Locate every blood parasite and identify its species.
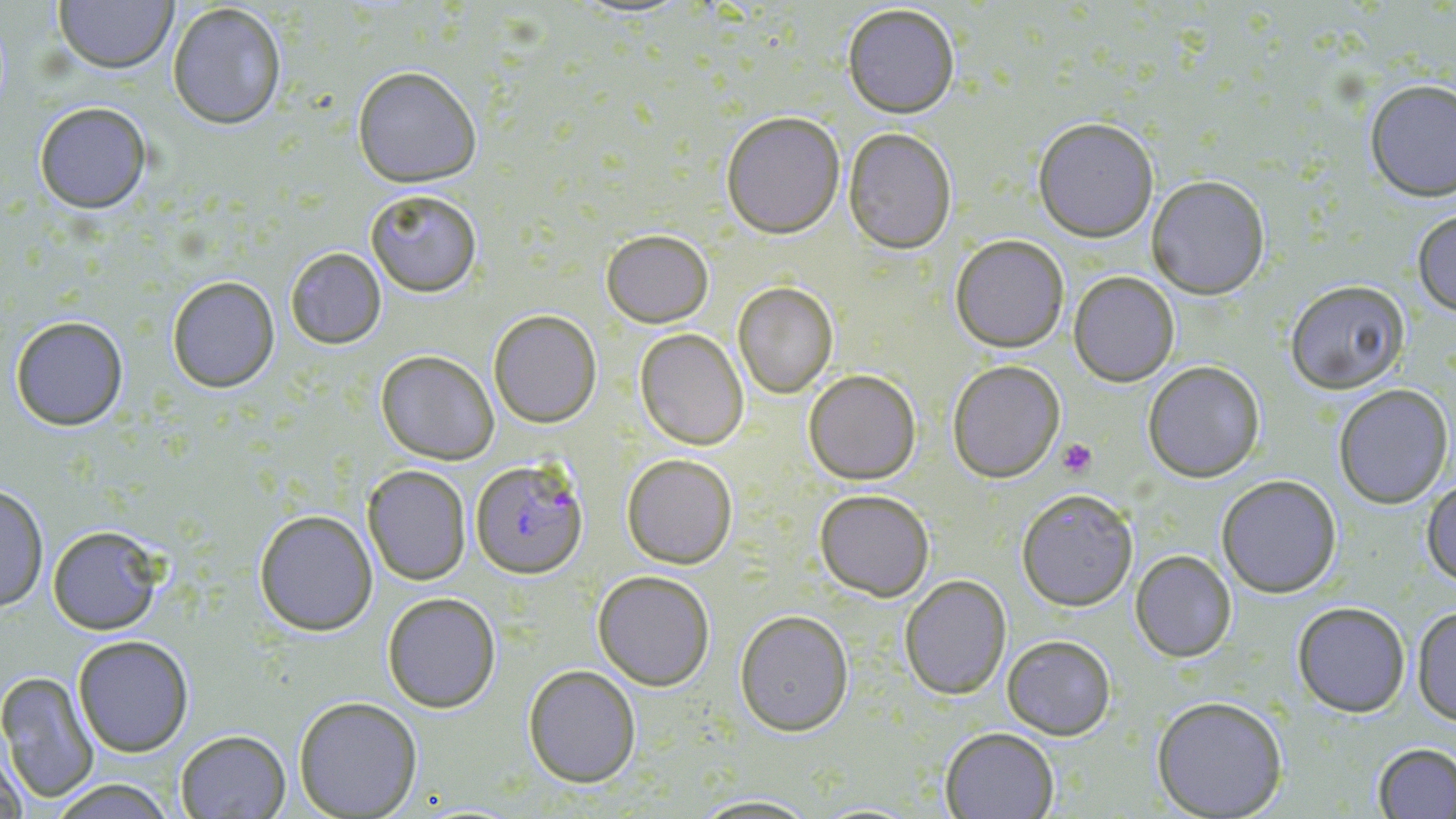
Approximate bounding boxes as (x1, y1, x2, y2) in pixels.
Plasmodium falciparum-infected red blood cells: (471, 458, 588, 578).
No Plasmodium ovale, Plasmodium malariae, Plasmodium vivax, Babesia divergens, or Trypanosoma brucei observed.

slide_level_diagnosis: Plasmodium falciparum
magnification: 1000x
preparation: thin blood film
uninfected_red_blood_cell_locations: 'approximate bounding boxes as (x1, y1, x2, y2) in pixels: (54, 0, 178, 74), (167, 3, 288, 130), (842, 3, 961, 117), (352, 65, 482, 187), (1364, 78, 1456, 201), (33, 101, 152, 213), (720, 111, 845, 238), (1033, 116, 1159, 242), (843, 127, 957, 254), (1147, 175, 1270, 299), (365, 188, 482, 296), (1412, 208, 1456, 317), (602, 229, 713, 328), (950, 234, 1069, 352), (285, 247, 386, 349), (1069, 271, 1179, 386), (166, 275, 280, 392), (1285, 279, 1409, 393), (732, 282, 838, 398), (489, 309, 602, 427), (10, 315, 129, 431), (634, 329, 749, 450), (376, 350, 499, 465), (947, 359, 1065, 482), (1142, 360, 1265, 482), (803, 369, 921, 485), (1333, 383, 1454, 509), (622, 453, 738, 568), (363, 464, 471, 586), (1216, 474, 1342, 598), (1422, 476, 1456, 586), (0, 483, 49, 612), (1017, 488, 1138, 611), (814, 489, 934, 601), (254, 509, 378, 636), (47, 525, 163, 634), (1130, 550, 1236, 662), (593, 570, 715, 690), (899, 574, 1011, 700), (382, 591, 501, 713), (1293, 601, 1411, 717), (1411, 605, 1456, 726), (735, 609, 854, 735), (1002, 634, 1116, 740), (72, 635, 194, 757), (523, 664, 641, 787), (0, 671, 99, 803), (1151, 695, 1288, 818), (293, 696, 423, 818), (940, 727, 1059, 819), (174, 729, 291, 818), (0, 741, 27, 819), (1373, 742, 1456, 818), (46, 778, 178, 818), (688, 794, 823, 818)'
stain: May-Grünwald-Giemsa
modality: optical microscopy
platelet_locations: 'approximate bounding boxes as (x1, y1, x2, y2) in pixels: (1056, 438, 1097, 478)'
field_of_view: one of a larger specimen
image_size: 1456×819 pixels